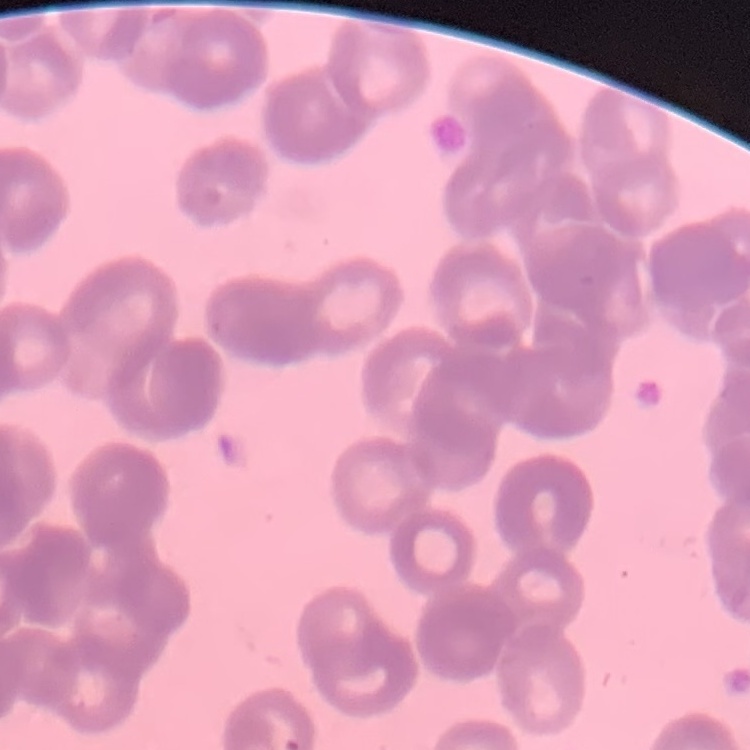

red blood cell morphology = rouleaux formation
image type = one tile cut from a larger photomicrograph
stain = Field's or Giemsa
preparation = thin blood smear